Locate every blood parasite and identify its species.
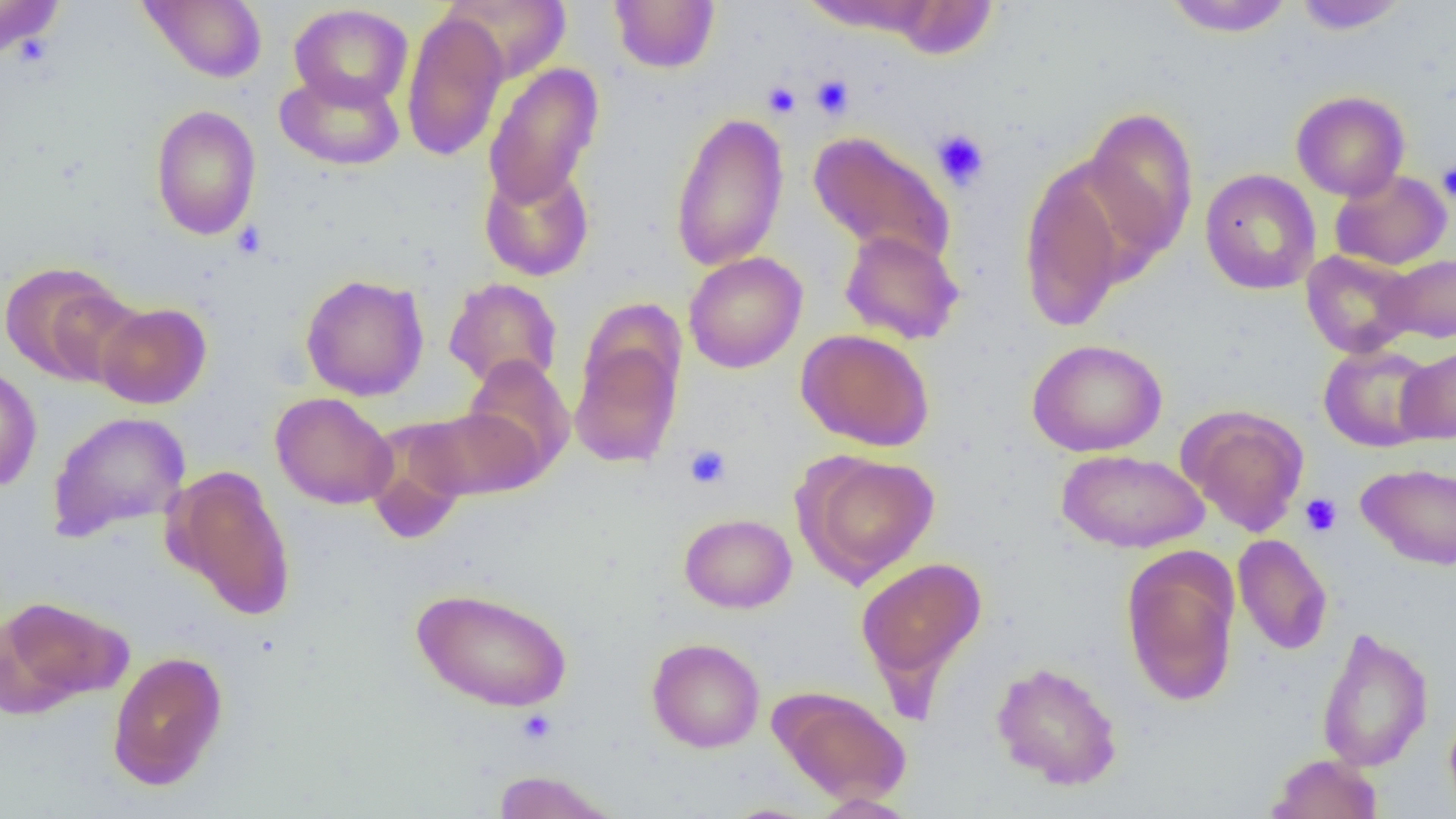

No blood parasites observed.

slide-level diagnosis = negative for blood parasites
field of view = single
modality = light microscopy
uninfected red blood cell locations = approximate bounding boxes as [x1, y1, x2, y2] in pixels: [0, 0, 64, 62], [138, 0, 268, 83], [442, 0, 571, 83], [609, 0, 720, 74], [1163, 0, 1294, 37], [1292, 0, 1409, 34], [799, 1, 941, 36], [890, 1, 998, 60], [289, 4, 413, 109], [400, 10, 509, 162], [484, 63, 603, 208], [275, 70, 405, 171], [1291, 91, 1410, 201], [150, 104, 262, 240], [1081, 106, 1199, 266], [669, 111, 789, 272], [807, 130, 957, 266], [1017, 158, 1138, 332], [478, 162, 594, 282], [1200, 168, 1321, 294], [1329, 170, 1452, 270], [839, 229, 964, 345], [1301, 250, 1419, 359], [684, 251, 808, 373], [1379, 253, 1456, 344], [1, 261, 138, 385], [300, 273, 429, 401], [444, 277, 562, 390], [95, 302, 212, 409], [796, 329, 935, 452], [1026, 338, 1167, 457], [569, 339, 682, 468], [1318, 344, 1440, 452], [1395, 345, 1456, 444], [462, 355, 575, 479], [0, 366, 42, 492], [270, 393, 398, 510], [1181, 405, 1309, 536], [413, 407, 543, 500], [47, 411, 191, 542], [363, 417, 473, 545], [1056, 449, 1209, 553], [797, 452, 941, 584], [1356, 463, 1456, 570], [165, 465, 297, 620], [679, 512, 797, 613], [1233, 534, 1332, 655], [1121, 548, 1239, 707], [855, 557, 987, 692], [411, 586, 574, 712], [0, 595, 129, 714], [1316, 626, 1434, 772], [646, 637, 765, 753], [107, 650, 229, 791], [990, 660, 1123, 790], [770, 686, 911, 805], [1444, 704, 1456, 817], [1267, 753, 1383, 819], [490, 770, 619, 818], [808, 793, 919, 818], [717, 803, 825, 819]
preparation = thin blood smear
image size = 1456×819 pixels
platelet locations = approximate bounding boxes as [x1, y1, x2, y2] in pixels: [810, 74, 855, 120], [763, 81, 801, 118], [931, 128, 991, 191], [1436, 159, 1456, 204], [232, 221, 268, 260], [684, 445, 731, 489], [1300, 493, 1343, 538], [515, 709, 558, 744]
magnification = 1000x